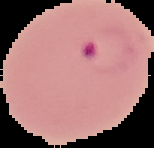

Summary:
  - Malaria status: parasitized
  - Image size: 154×148 pixels
  - Image type: segmented cell region with the area outside set to black
  - Preparation: thin blood film